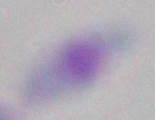
Summary:
  - Magnification: 1000x
  - Modality: micrograph
  - Identification: Toxoplasma gondii